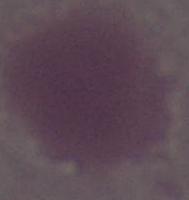

Summary:
  - Magnification: 1000x
  - Modality: micrograph
  - Identification: erythrocyte